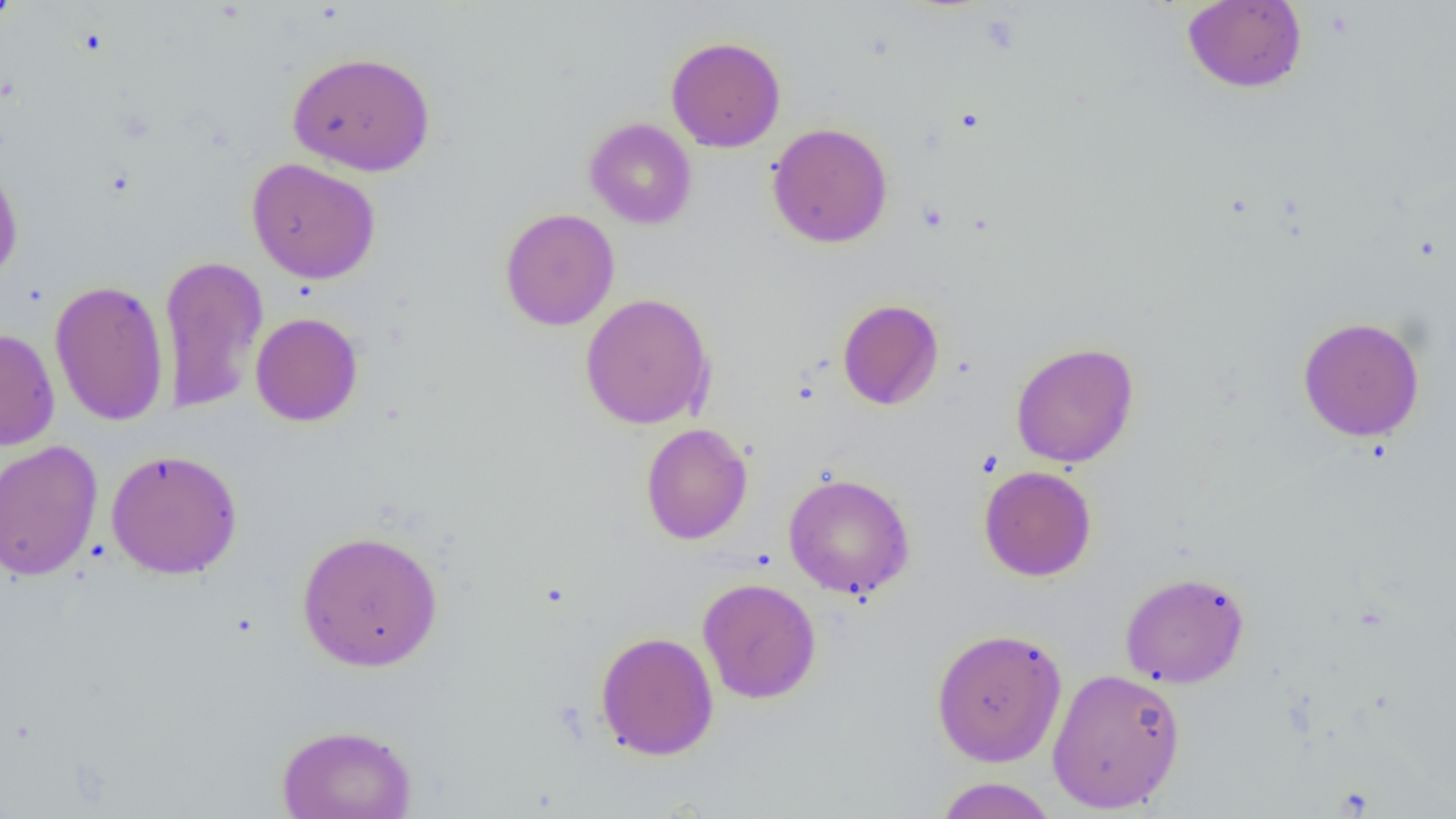

Summary:
  - Coordinate format: approximate bounding boxes as named x1/y1/x2/y2 corners in pixels
  - Uninfected red blood cell locations: (x1=0, y1=0, x2=23, y2=29), (x1=1182, y1=1, x2=1307, y2=93), (x1=666, y1=36, x2=785, y2=152), (x1=287, y1=51, x2=437, y2=176), (x1=584, y1=117, x2=697, y2=229), (x1=767, y1=122, x2=893, y2=248), (x1=0, y1=155, x2=24, y2=286), (x1=246, y1=157, x2=381, y2=284), (x1=499, y1=208, x2=620, y2=331), (x1=158, y1=254, x2=268, y2=414), (x1=49, y1=279, x2=170, y2=427), (x1=579, y1=293, x2=715, y2=430), (x1=837, y1=299, x2=944, y2=411), (x1=250, y1=312, x2=364, y2=427), (x1=1297, y1=316, x2=1426, y2=442), (x1=0, y1=328, x2=60, y2=451), (x1=1010, y1=341, x2=1139, y2=469), (x1=640, y1=423, x2=753, y2=544), (x1=0, y1=439, x2=103, y2=581), (x1=105, y1=448, x2=243, y2=580), (x1=978, y1=465, x2=1097, y2=581), (x1=783, y1=472, x2=915, y2=599), (x1=296, y1=529, x2=444, y2=672), (x1=1119, y1=571, x2=1250, y2=688), (x1=697, y1=577, x2=822, y2=704), (x1=930, y1=626, x2=1068, y2=767), (x1=595, y1=631, x2=719, y2=761), (x1=1047, y1=667, x2=1185, y2=814), (x1=276, y1=723, x2=418, y2=819), (x1=932, y1=777, x2=1059, y2=819)
  - Slide-level diagnosis: no evidence of blood parasites
  - Image size: 1456×819 pixels
  - Magnification: 1000x
  - Modality: light microscopy
  - Field of view: one of a larger specimen
  - Preparation: thin blood film